Assess this cell for malaria.
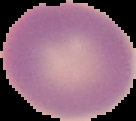
It is uninfected.

Summary:
  - Image type: segmented cell region with the area outside set to black
  - Preparation: thin blood film
  - Image size: 136×121 pixels